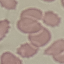
Summary:
  - Result: no malaria parasites detected
  - Capture: smartphone through the microscope eyepiece
  - Stain: Giemsa
  - Image type: automatically extracted cell patch, resized to 64 × 64 pixels
  - Preparation: thin smear